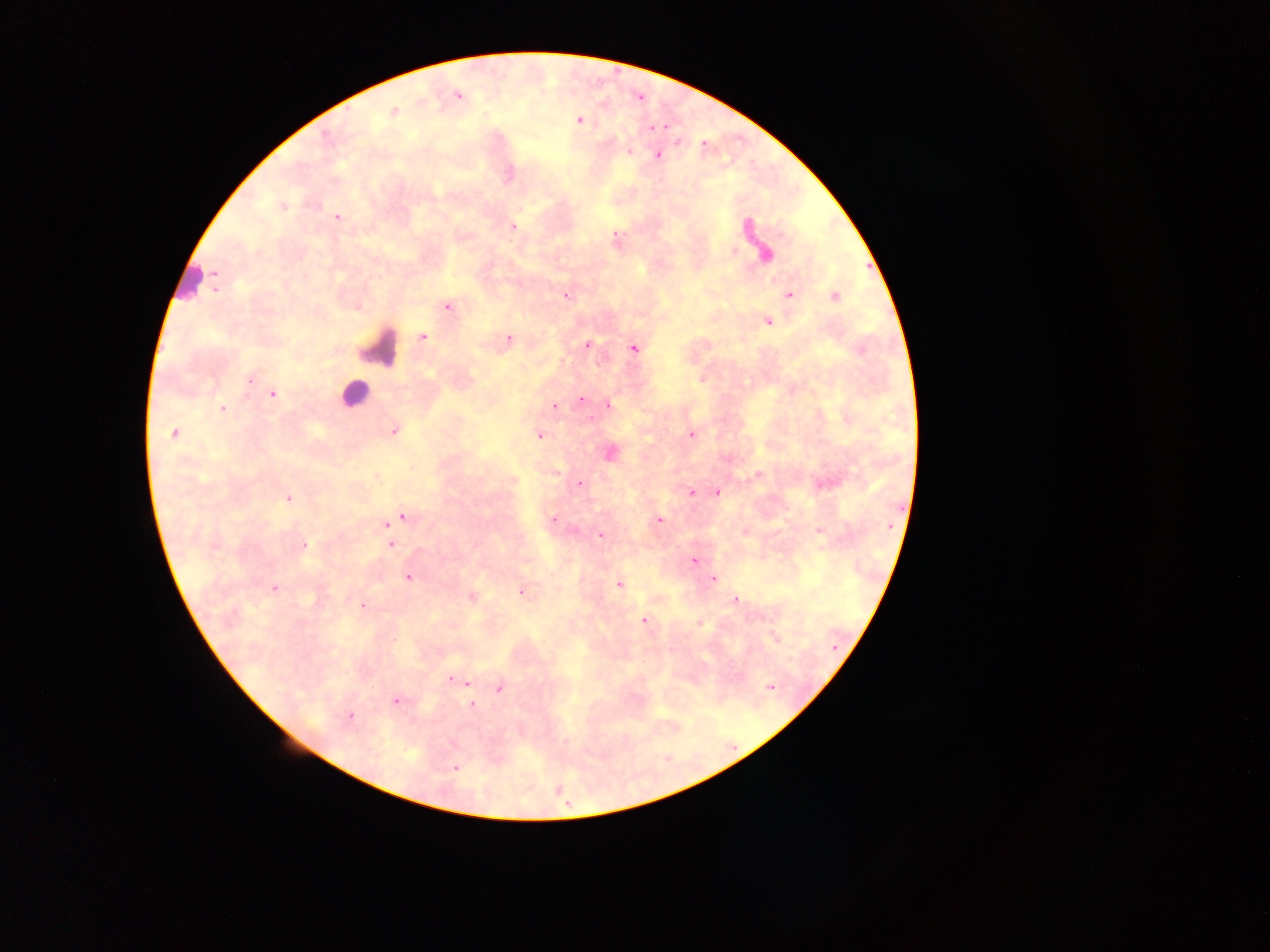

capture = mobile-phone photograph through a microscope
preparation = thick blood smear
malaria parasite locations = approximate centers as [x, y] in pixels: [457, 96], [393, 113], [578, 121], [655, 127], [626, 154], [657, 154], [511, 174], [284, 208], [336, 217], [744, 223], [513, 227], [780, 233], [614, 236], [733, 249], [765, 253], [565, 295], [786, 296], [833, 296], [449, 305], [357, 307], [769, 322], [423, 338], [509, 338], [589, 343], [633, 349], [701, 376], [249, 380], [273, 393], [581, 400], [608, 405], [552, 407], [224, 408], [393, 432], [173, 433], [691, 435], [538, 436], [610, 453], [726, 458], [554, 471], [758, 473], [375, 478], [513, 480], [579, 484], [691, 493], [717, 493], [290, 498], [403, 516], [552, 518], [659, 519], [384, 526], [819, 532], [744, 534], [600, 536], [305, 545], [391, 546], [692, 561], [408, 577], [713, 580], [618, 584], [274, 589], [519, 592], [472, 597], [734, 599], [361, 605], [644, 621], [701, 624], [452, 679], [465, 682], [498, 689], [396, 702], [472, 705], [564, 743], [456, 769]
image size = 1270×952 pixels
leukocyte locations = approximate centers as [x, y] in pixels: [190, 286], [380, 346], [358, 396]
field of view = single
country = Ghana